Locate every blood parasite and identify its species.
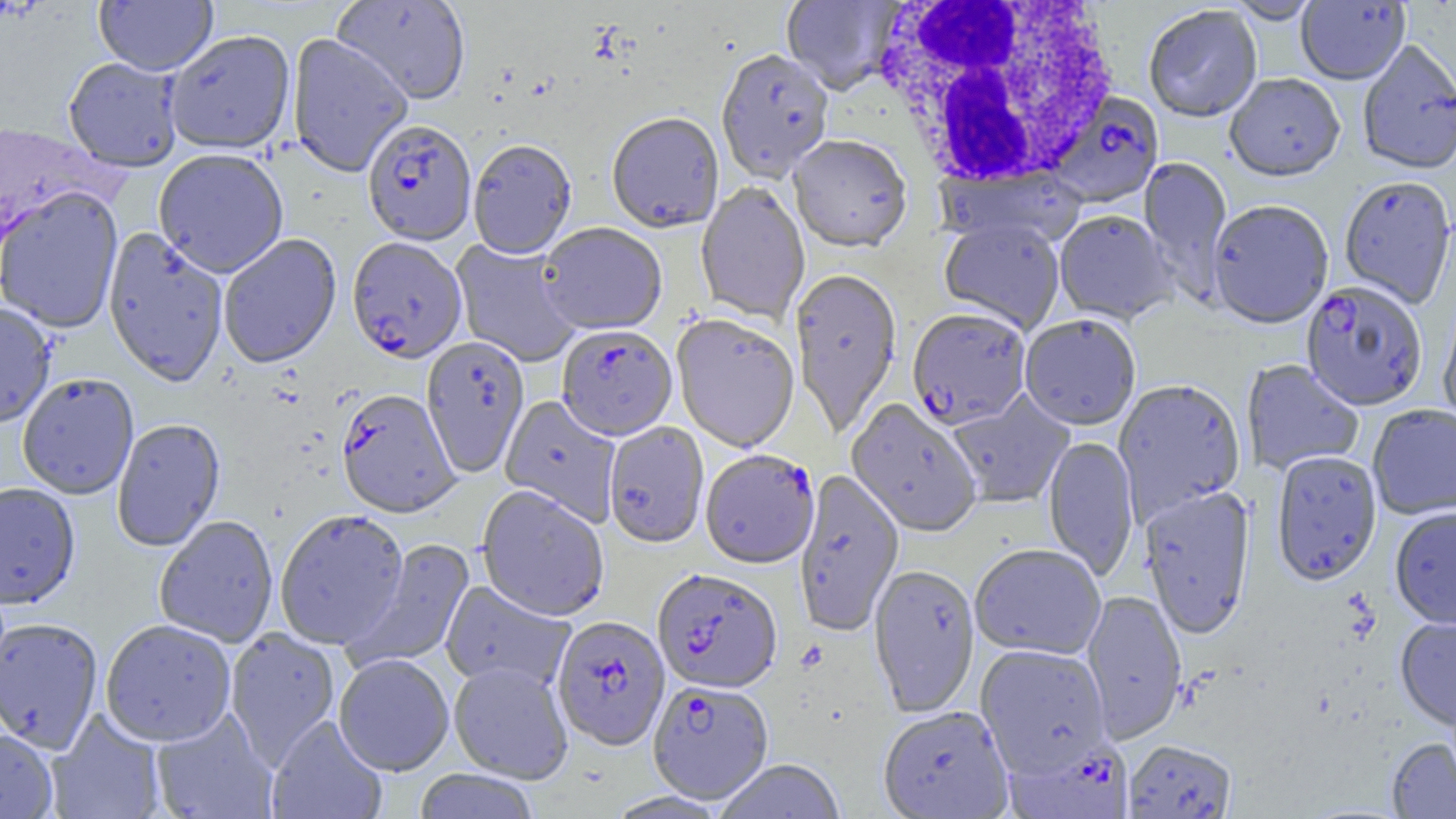

Approximate bounding boxes as named x1/y1/x2/y2 corners in pixels.
Plasmodium falciparum-infected red blood cells: (x1=1046, y1=87, x2=1166, y2=205), (x1=362, y1=121, x2=477, y2=247), (x1=347, y1=239, x2=467, y2=365), (x1=1301, y1=282, x2=1428, y2=413), (x1=907, y1=310, x2=1031, y2=431), (x1=556, y1=327, x2=678, y2=443), (x1=336, y1=391, x2=460, y2=520), (x1=700, y1=451, x2=820, y2=571), (x1=652, y1=569, x2=782, y2=695), (x1=552, y1=617, x2=670, y2=752), (x1=648, y1=680, x2=774, y2=805), (x1=1004, y1=738, x2=1134, y2=819).
No Plasmodium ovale, Plasmodium malariae, Plasmodium vivax, Babesia divergens, or Trypanosoma brucei observed.

White blood cell locations: (x1=867, y1=0, x2=1121, y2=190). Uninfected red blood cell locations: (x1=94, y1=0, x2=217, y2=76), (x1=332, y1=0, x2=470, y2=106), (x1=781, y1=0, x2=902, y2=96), (x1=1296, y1=0, x2=1410, y2=87), (x1=1225, y1=1, x2=1322, y2=25), (x1=1144, y1=7, x2=1262, y2=125), (x1=164, y1=30, x2=296, y2=156), (x1=287, y1=33, x2=413, y2=178), (x1=1358, y1=40, x2=1456, y2=177), (x1=716, y1=50, x2=834, y2=184), (x1=63, y1=58, x2=183, y2=173), (x1=1224, y1=75, x2=1345, y2=185), (x1=607, y1=114, x2=724, y2=234), (x1=1, y1=117, x2=103, y2=253), (x1=788, y1=137, x2=912, y2=255), (x1=468, y1=141, x2=577, y2=261), (x1=153, y1=149, x2=289, y2=278), (x1=1139, y1=156, x2=1233, y2=301), (x1=935, y1=166, x2=1087, y2=250), (x1=1339, y1=177, x2=1456, y2=310), (x1=696, y1=184, x2=810, y2=326), (x1=0, y1=187, x2=124, y2=333), (x1=1208, y1=202, x2=1333, y2=331), (x1=1054, y1=211, x2=1177, y2=326), (x1=939, y1=219, x2=1065, y2=335), (x1=538, y1=224, x2=667, y2=337), (x1=103, y1=229, x2=229, y2=387), (x1=218, y1=235, x2=341, y2=369), (x1=450, y1=239, x2=582, y2=368), (x1=790, y1=269, x2=903, y2=438), (x1=1438, y1=300, x2=1456, y2=434), (x1=0, y1=303, x2=56, y2=428), (x1=671, y1=315, x2=800, y2=455), (x1=1019, y1=316, x2=1141, y2=432), (x1=421, y1=337, x2=529, y2=479), (x1=1241, y1=359, x2=1364, y2=476), (x1=17, y1=373, x2=139, y2=501), (x1=1113, y1=379, x2=1247, y2=526), (x1=947, y1=392, x2=1075, y2=509), (x1=500, y1=395, x2=621, y2=527), (x1=845, y1=399, x2=982, y2=538), (x1=1367, y1=405, x2=1456, y2=521), (x1=112, y1=420, x2=226, y2=553), (x1=604, y1=423, x2=709, y2=551), (x1=1043, y1=436, x2=1138, y2=581), (x1=1272, y1=451, x2=1382, y2=587), (x1=794, y1=470, x2=903, y2=638), (x1=0, y1=482, x2=81, y2=610), (x1=1140, y1=486, x2=1256, y2=641), (x1=476, y1=487, x2=609, y2=622), (x1=1390, y1=507, x2=1456, y2=631), (x1=274, y1=510, x2=410, y2=650), (x1=154, y1=516, x2=279, y2=648), (x1=346, y1=539, x2=476, y2=672), (x1=970, y1=545, x2=1106, y2=661), (x1=868, y1=566, x2=979, y2=718), (x1=440, y1=581, x2=576, y2=694), (x1=1081, y1=591, x2=1186, y2=744), (x1=1395, y1=617, x2=1456, y2=733), (x1=0, y1=618, x2=103, y2=754), (x1=100, y1=620, x2=236, y2=747), (x1=225, y1=628, x2=340, y2=768), (x1=974, y1=644, x2=1111, y2=777), (x1=334, y1=654, x2=454, y2=777), (x1=448, y1=662, x2=573, y2=784), (x1=877, y1=706, x2=1014, y2=819), (x1=46, y1=709, x2=166, y2=819), (x1=150, y1=709, x2=278, y2=819), (x1=266, y1=716, x2=387, y2=819), (x1=0, y1=728, x2=59, y2=818), (x1=1386, y1=738, x2=1456, y2=818), (x1=1123, y1=740, x2=1237, y2=818), (x1=713, y1=759, x2=847, y2=819), (x1=413, y1=769, x2=540, y2=819), (x1=606, y1=791, x2=731, y2=819). Slide-level diagnosis: Plasmodium falciparum. Thin blood smear. Single field of view. Image is 1456×819 pixels. 1000x magnification. Optical microscopy.